Identify the parasite.
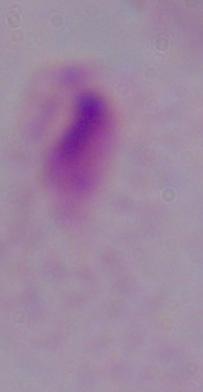
A trichomonad.

{
  "modality": "photomicrograph",
  "magnification": "1000x"
}